Outline platelets.
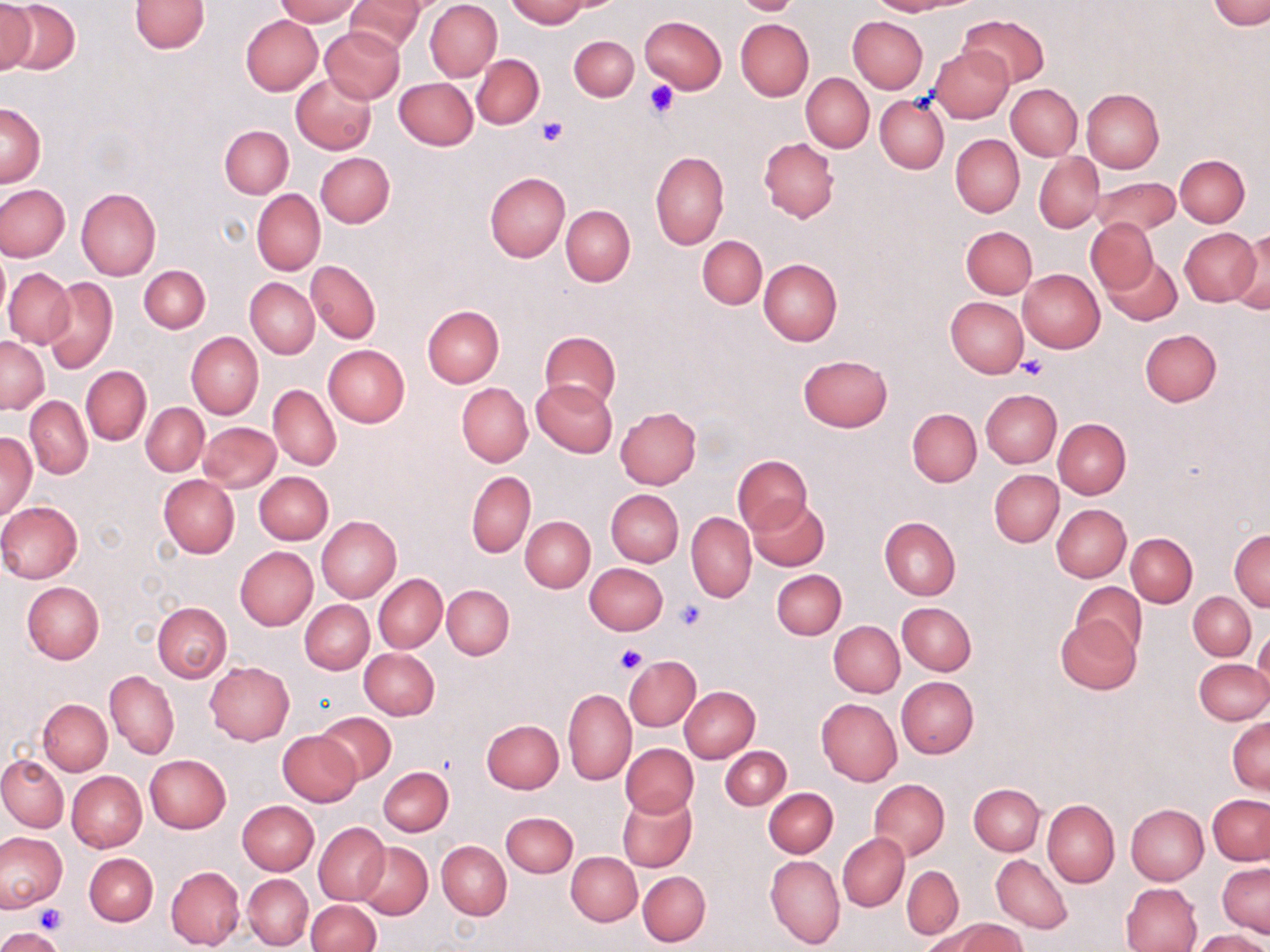

Approximate bounding boxes as [x1, y1, x2, y2] in pixels.
Platelets: [644, 79, 679, 118], [535, 116, 568, 145], [1017, 355, 1049, 380], [675, 600, 705, 631], [613, 645, 648, 675], [36, 902, 66, 935].

Summary:
  - Uninfected red blood cell locations: [1, 0, 79, 76], [131, 0, 209, 54], [274, 0, 362, 25], [506, 0, 590, 27], [556, 0, 623, 11], [733, 0, 800, 15], [868, 0, 962, 15], [1210, 0, 1269, 29], [347, 1, 426, 54], [425, 1, 501, 81], [0, 2, 36, 76], [959, 13, 1047, 87], [241, 15, 323, 96], [640, 16, 727, 93], [847, 16, 927, 93], [735, 18, 813, 100], [320, 26, 404, 103], [570, 35, 638, 101], [929, 44, 1013, 123], [472, 54, 544, 129], [801, 72, 874, 152], [291, 73, 377, 153], [393, 78, 478, 150], [1006, 83, 1082, 160], [1081, 89, 1164, 172], [875, 95, 949, 174], [0, 103, 46, 187], [220, 125, 293, 198], [950, 134, 1025, 217], [759, 138, 839, 222], [650, 150, 730, 250], [316, 152, 394, 227], [1034, 153, 1103, 231], [1175, 155, 1249, 227], [486, 173, 570, 262], [1088, 177, 1179, 238], [0, 184, 70, 263], [75, 187, 161, 280], [251, 189, 326, 275], [561, 205, 635, 286], [1086, 217, 1158, 294], [961, 226, 1036, 299], [1179, 227, 1260, 306], [1230, 230, 1270, 312], [698, 236, 766, 309], [694, 243, 826, 320], [0, 251, 10, 321], [1101, 254, 1182, 326], [759, 259, 841, 347], [306, 260, 380, 343], [139, 264, 210, 333], [4, 267, 75, 349], [1017, 269, 1104, 353], [41, 276, 118, 374], [245, 278, 319, 358], [946, 296, 1028, 377], [422, 305, 504, 387], [1139, 329, 1221, 406], [540, 331, 621, 409], [186, 332, 263, 419], [1, 336, 49, 413], [323, 344, 410, 426], [798, 354, 892, 431], [80, 366, 151, 445], [531, 379, 617, 457], [457, 383, 533, 467], [268, 385, 340, 471], [981, 389, 1061, 467], [25, 397, 93, 478], [141, 403, 208, 475], [614, 406, 701, 489], [907, 408, 981, 488], [1053, 418, 1131, 499], [199, 422, 280, 491], [1, 432, 37, 521], [733, 454, 812, 535], [466, 470, 535, 558], [989, 470, 1063, 546], [254, 471, 332, 544], [157, 474, 240, 558], [606, 489, 684, 567], [748, 497, 830, 572], [0, 501, 83, 584], [1052, 504, 1130, 581], [687, 513, 756, 601], [315, 516, 401, 602], [522, 516, 595, 592], [879, 517, 960, 600], [1229, 530, 1270, 611], [1127, 533, 1198, 606], [234, 546, 317, 631], [584, 562, 668, 634], [772, 569, 846, 638], [374, 574, 447, 653], [22, 582, 104, 664], [1070, 582, 1147, 656], [442, 585, 514, 660], [1189, 592, 1255, 660], [300, 600, 374, 673], [153, 602, 232, 682], [897, 602, 976, 674], [831, 613, 977, 692], [1056, 616, 1141, 695], [829, 621, 905, 697], [1253, 627, 1270, 701], [359, 648, 440, 720], [622, 653, 703, 731], [1195, 659, 1270, 725], [205, 661, 294, 744], [105, 670, 178, 758], [896, 676, 979, 758], [678, 686, 759, 762], [562, 687, 636, 785], [38, 698, 112, 775], [816, 698, 902, 785], [317, 711, 396, 784], [1228, 718, 1269, 793], [482, 719, 564, 793], [277, 730, 362, 806], [621, 743, 698, 817], [721, 746, 791, 810], [145, 754, 231, 833], [0, 755, 67, 831], [378, 766, 453, 836], [68, 771, 146, 852], [868, 779, 949, 861], [968, 783, 1045, 856], [765, 788, 837, 856], [616, 792, 696, 873], [1208, 794, 1270, 864], [1043, 799, 1119, 887], [237, 800, 319, 874], [1125, 804, 1209, 884], [501, 812, 577, 877], [314, 822, 390, 904], [0, 832, 66, 912], [838, 833, 909, 911], [437, 841, 511, 920], [355, 842, 432, 920], [567, 851, 641, 926], [84, 853, 157, 926], [765, 854, 845, 949], [991, 854, 1072, 934], [1217, 862, 1270, 939], [903, 865, 963, 939], [165, 866, 244, 951], [638, 870, 710, 946], [243, 873, 313, 950], [1122, 882, 1203, 952], [307, 901, 380, 952], [935, 918, 1026, 952], [0, 929, 63, 952], [1193, 930, 1270, 952]
  - Slide-level diagnosis: no evidence of blood parasites
  - Magnification: 1000x
  - Stain: May-Grünwald-Giemsa
  - Preparation: thin blood smear
  - Image size: 1270×952 pixels
  - Modality: light microscopy
  - Field of view: single